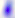 400x magnification. Toxoplasma gondii is shown. Photomicrograph.